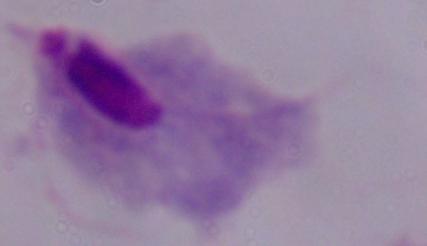

{
  "modality": "micrograph",
  "magnification": "1000x",
  "identification": "trichomonad"
}